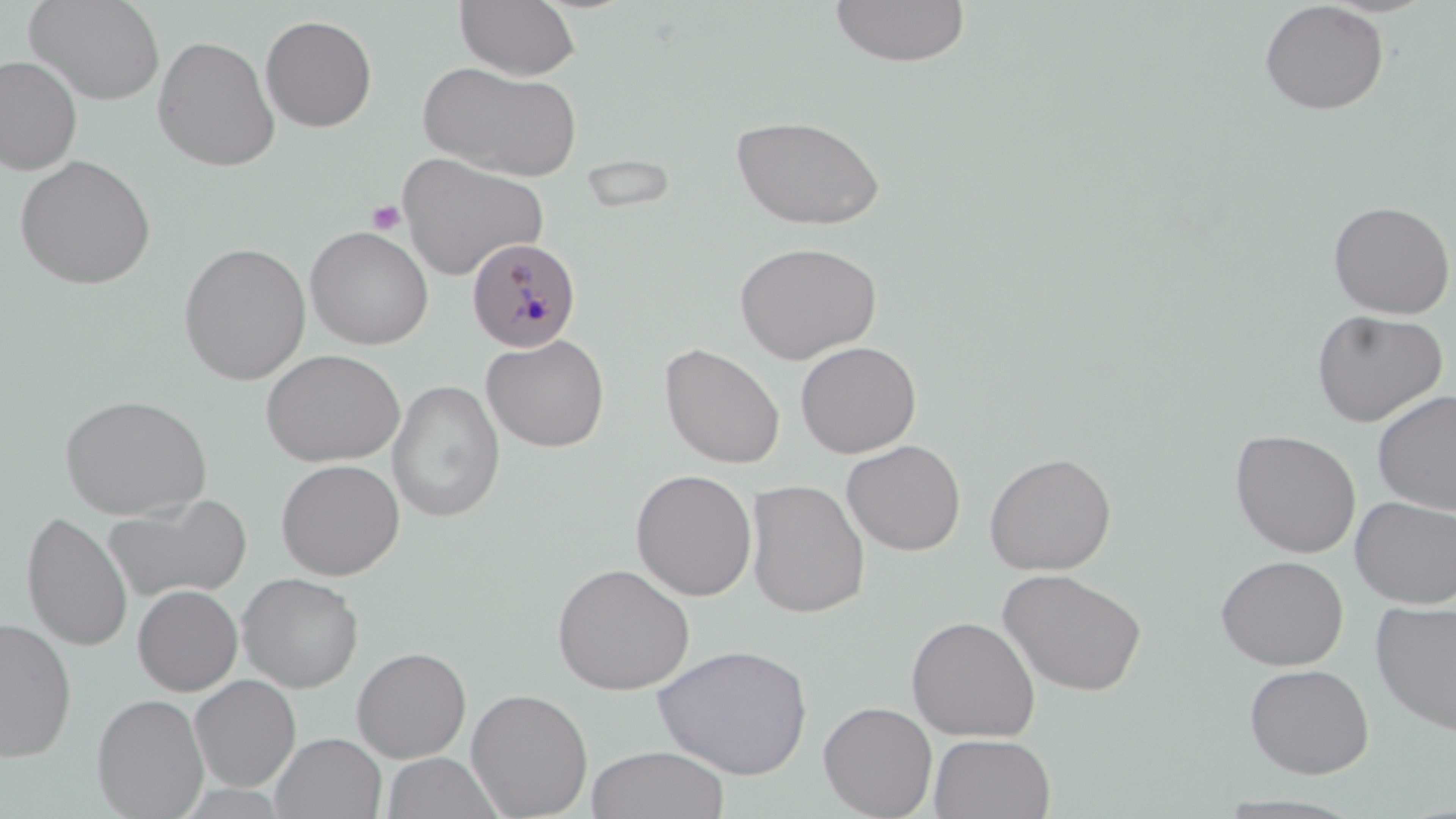

slide_level_diagnosis: Plasmodium malariae
uninfected_red_blood_cell_locations: 'approximate bounding boxes as (x1, y1, x2, y2) in pixels: (26, 0, 165, 105), (454, 0, 581, 80), (828, 1, 971, 68), (1259, 1, 1389, 116), (260, 14, 377, 132), (152, 35, 280, 171), (0, 55, 82, 175), (417, 60, 584, 181), (730, 114, 885, 231), (396, 152, 548, 280), (14, 155, 156, 290), (1328, 200, 1455, 319), (304, 225, 434, 350), (733, 240, 882, 363), (178, 243, 311, 385), (1311, 309, 1447, 427), (481, 334, 610, 452), (794, 340, 921, 458), (659, 342, 785, 469), (260, 349, 405, 467), (388, 379, 504, 523), (1372, 389, 1456, 515), (58, 393, 212, 520), (1230, 429, 1361, 558), (841, 439, 966, 556), (983, 451, 1117, 575), (275, 458, 405, 580), (631, 468, 757, 601), (745, 479, 870, 619), (104, 493, 253, 604), (1350, 496, 1456, 609), (22, 509, 132, 653), (1215, 554, 1349, 670), (551, 562, 695, 695), (997, 567, 1148, 697), (237, 573, 364, 692), (132, 584, 243, 696), (1370, 599, 1456, 736), (906, 615, 1040, 742), (0, 618, 77, 763), (652, 643, 813, 780), (352, 646, 471, 763), (1243, 663, 1375, 778), (189, 675, 301, 791), (466, 688, 593, 818), (92, 693, 208, 818), (818, 700, 938, 818), (270, 732, 387, 819), (928, 733, 1056, 819), (586, 746, 732, 819), (380, 752, 505, 819)'
modality: light microscopy
plasmodium_malariae_infected_red_blood_cell_locations: 'approximate bounding boxes as (x1, y1, x2, y2) in pixels: (466, 237, 582, 353)'
preparation: thin blood film
field_of_view: one of a larger specimen
magnification: 1000x
image_size: 1456×819 pixels
stain: May-Grünwald-Giemsa
platelet_locations: 'approximate bounding boxes as (x1, y1, x2, y2) in pixels: (367, 200, 405, 236)'